Outline each uninfected red blood cell.
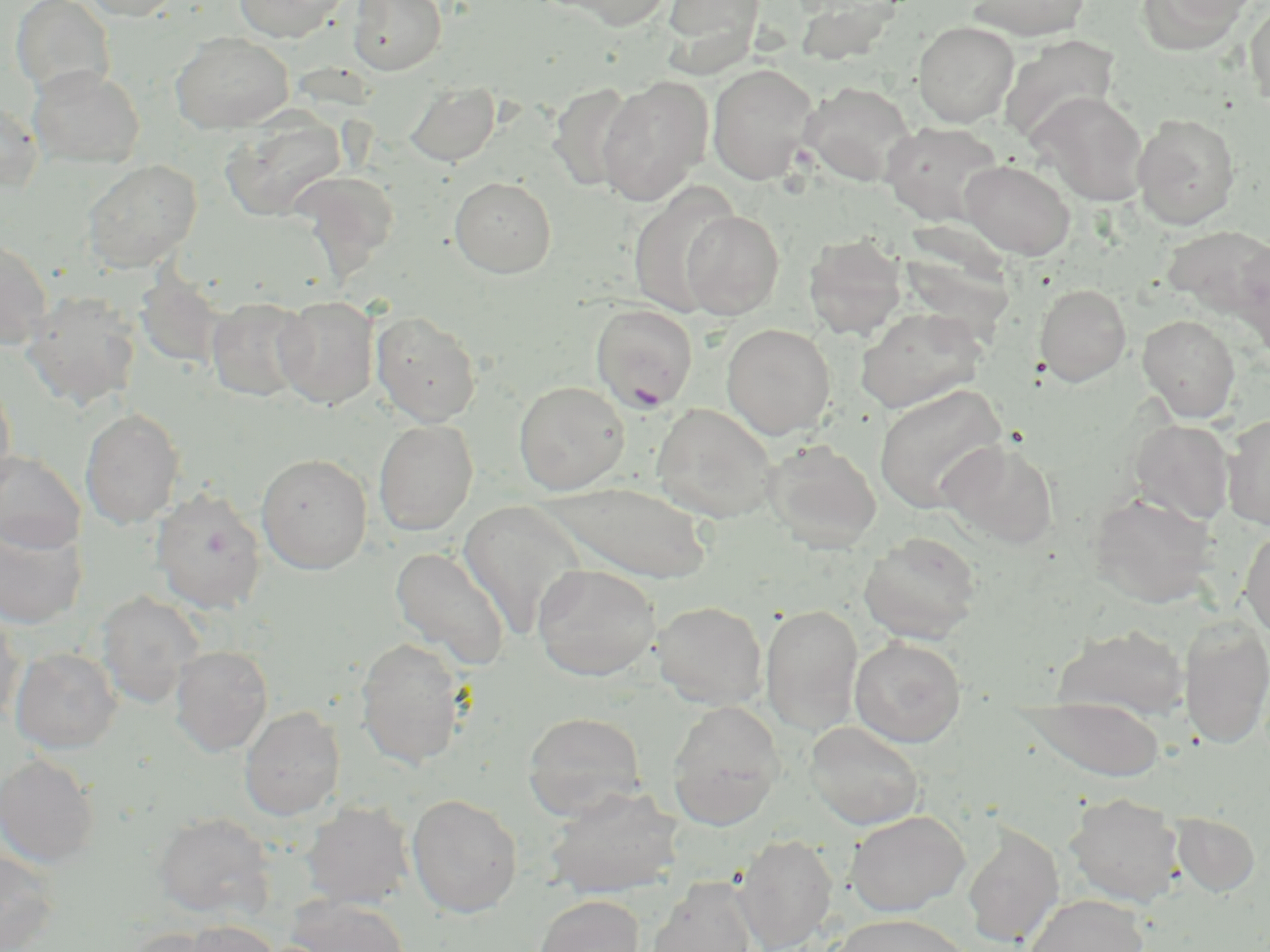
Approximate bounding boxes as (x1, y1, x2, y2) in pixels.
Uninfected red blood cells: (10, 0, 115, 98), (81, 0, 181, 20), (233, 0, 349, 42), (348, 0, 447, 76), (549, 0, 676, 30), (662, 0, 766, 65), (964, 0, 1092, 41), (1140, 0, 1258, 51), (1244, 3, 1270, 106), (913, 21, 1018, 127), (170, 31, 294, 133), (999, 35, 1120, 143), (707, 63, 818, 185), (28, 65, 144, 169), (596, 76, 713, 206), (800, 81, 916, 186), (406, 82, 499, 166), (549, 82, 639, 194), (1031, 91, 1150, 205), (0, 98, 44, 193), (1132, 112, 1241, 230), (220, 113, 348, 221), (881, 121, 1005, 226), (82, 159, 203, 273), (959, 159, 1075, 260), (292, 170, 401, 275), (450, 176, 557, 278), (628, 183, 742, 318), (681, 210, 785, 319), (803, 233, 906, 341), (0, 236, 53, 350), (1234, 238, 1270, 360), (134, 268, 227, 371), (1034, 283, 1131, 386), (22, 289, 142, 411), (275, 295, 379, 409), (206, 296, 312, 402), (856, 307, 988, 413), (372, 311, 481, 426), (1137, 314, 1241, 422), (721, 323, 836, 439), (0, 380, 16, 493), (513, 380, 630, 495), (873, 383, 1008, 515), (650, 403, 779, 523), (80, 407, 185, 530), (1221, 414, 1270, 530), (373, 418, 478, 535), (1129, 419, 1235, 526), (763, 438, 882, 553), (940, 440, 1060, 550), (0, 450, 86, 552), (256, 453, 373, 574), (545, 480, 713, 583), (150, 487, 267, 615), (1088, 491, 1218, 608), (458, 500, 589, 639), (0, 519, 88, 629), (1240, 526, 1270, 641), (859, 532, 981, 644), (389, 545, 510, 670), (532, 564, 660, 681), (96, 591, 204, 709), (653, 600, 768, 709), (761, 604, 864, 734), (0, 608, 24, 726), (1179, 617, 1270, 751), (1053, 624, 1189, 721), (355, 637, 467, 769), (849, 637, 967, 747), (169, 645, 273, 756), (10, 647, 122, 753), (1025, 695, 1166, 782), (667, 700, 784, 830), (240, 705, 345, 821), (522, 711, 645, 820), (804, 720, 926, 830), (0, 753, 100, 868), (544, 785, 683, 899), (1065, 792, 1184, 908), (406, 793, 522, 917), (301, 800, 416, 908), (845, 810, 970, 916), (153, 812, 274, 920), (1171, 812, 1260, 896), (962, 824, 1064, 947), (734, 834, 838, 951), (0, 849, 60, 951), (647, 876, 759, 952), (533, 894, 645, 952), (1024, 894, 1148, 952), (287, 895, 411, 952), (830, 913, 974, 951), (181, 919, 281, 952), (122, 927, 225, 952).

slide-level diagnosis = Plasmodium falciparum
preparation = thin blood smear
magnification = 1000x
field of view = single
modality = optical microscopy
Plasmodium falciparum-infected red blood cell locations = approximate bounding boxes as (x1, y1, x2, y2) in pixels: (590, 304, 699, 412)
stain = May-Grünwald-Giemsa
image size = 1270×952 pixels